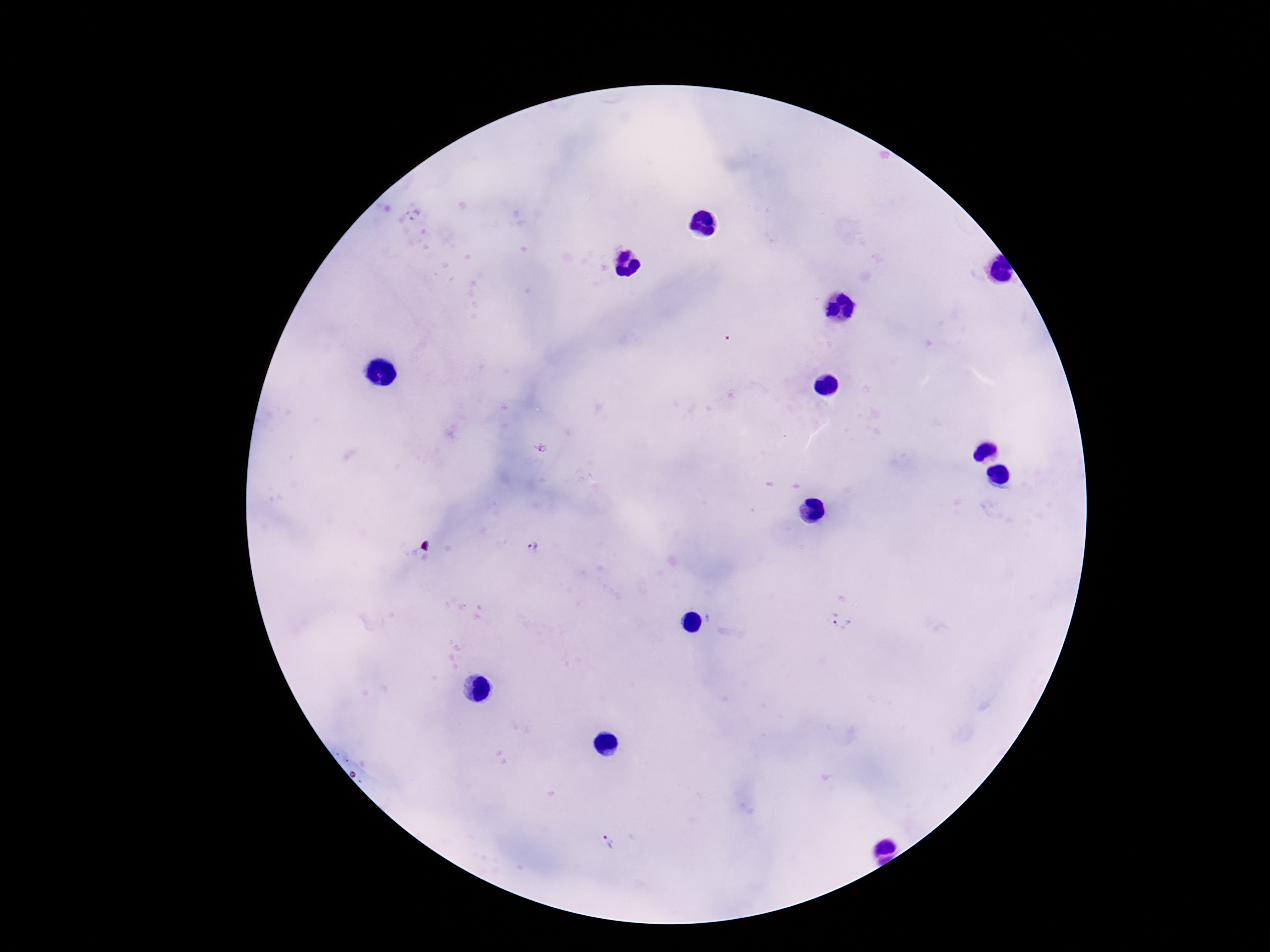

Approximate object centers, in pixels from the top-left corner. Plasmodium parasite locations: (x=413, y=215), (x=541, y=450), (x=532, y=547), (x=840, y=620), (x=609, y=843). One field from this slide. Giemsa stain. Patient malaria status: positive. Photographed through the microscope eyepiece with a smartphone camera. 100x magnification. Image is 1270×952 pixels. Thick peripheral-blood smear.